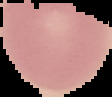 From a thin blood film. Cell region segmented out of the field of view; the surrounding area is masked to black. Image is 112×97 pixels. Result: no Plasmodium parasites seen.